Assess this cell for malaria.
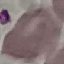
Uninfected.

Thin blood film. Giemsa-stained preparation. Cell patch, automatically extracted from a larger field of view and resized to 64 × 64 pixels. Photographed with a smartphone camera at the microscope eyepiece.